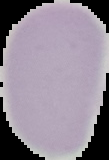
image type = segmented cell region with the area outside set to black
result = no malaria parasites detected
preparation = thin blood film
image size = 109×160 pixels